Assess for Plasmodium parasites.
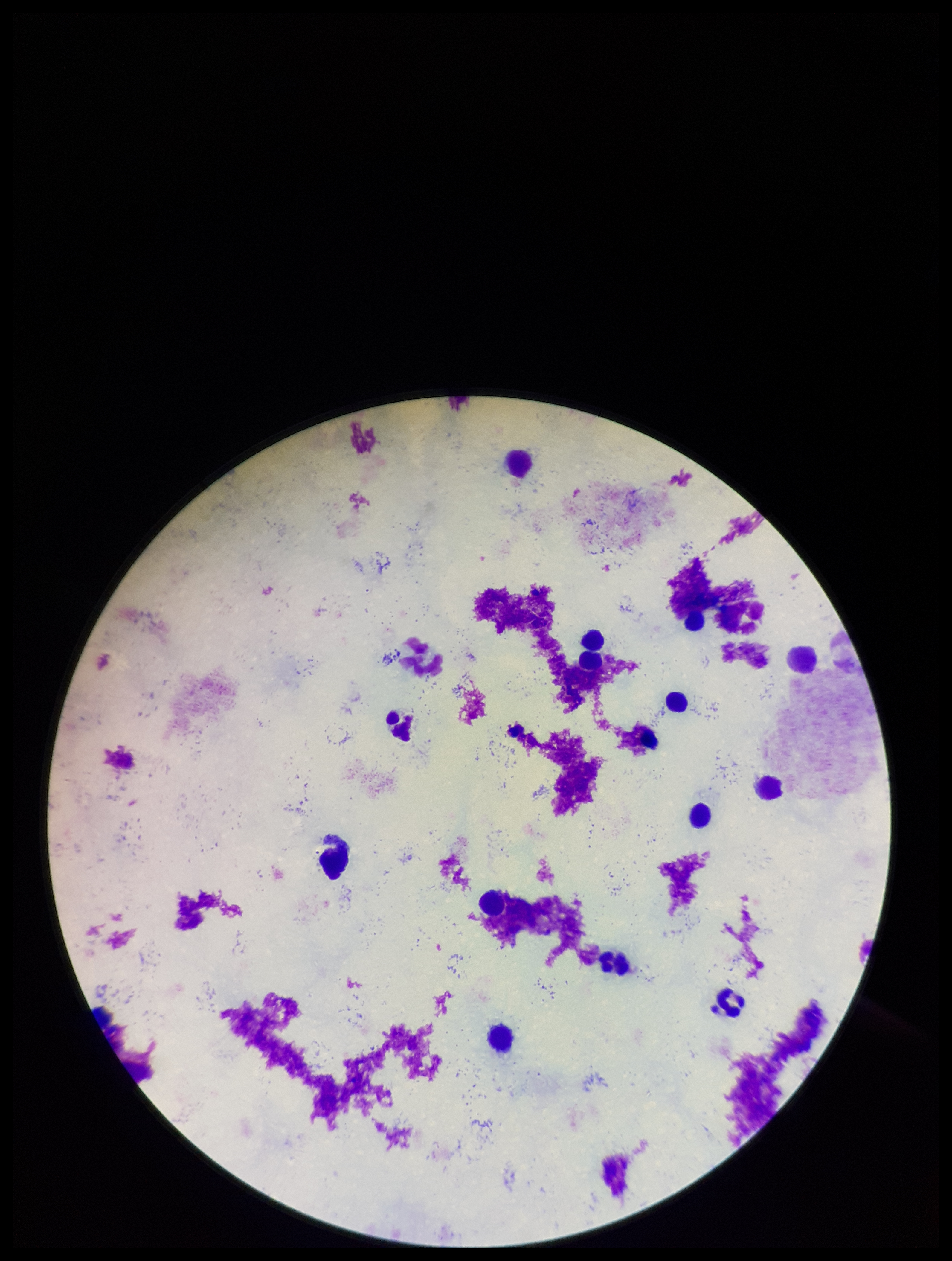
None detected.

One field from this slide. Preparation: thick. Patient malaria status: negative. Leukocyte count: 13. Smartphone photograph taken through the eyepiece of a microscope. Stained with Giemsa. Parasite count: 0. Image is 952×1261 pixels.